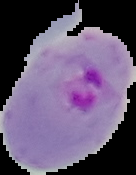

Image is 136×175 pixels. From a thin blood film. The area outside the segmented cell region is set to black. Result: malaria parasites detected.